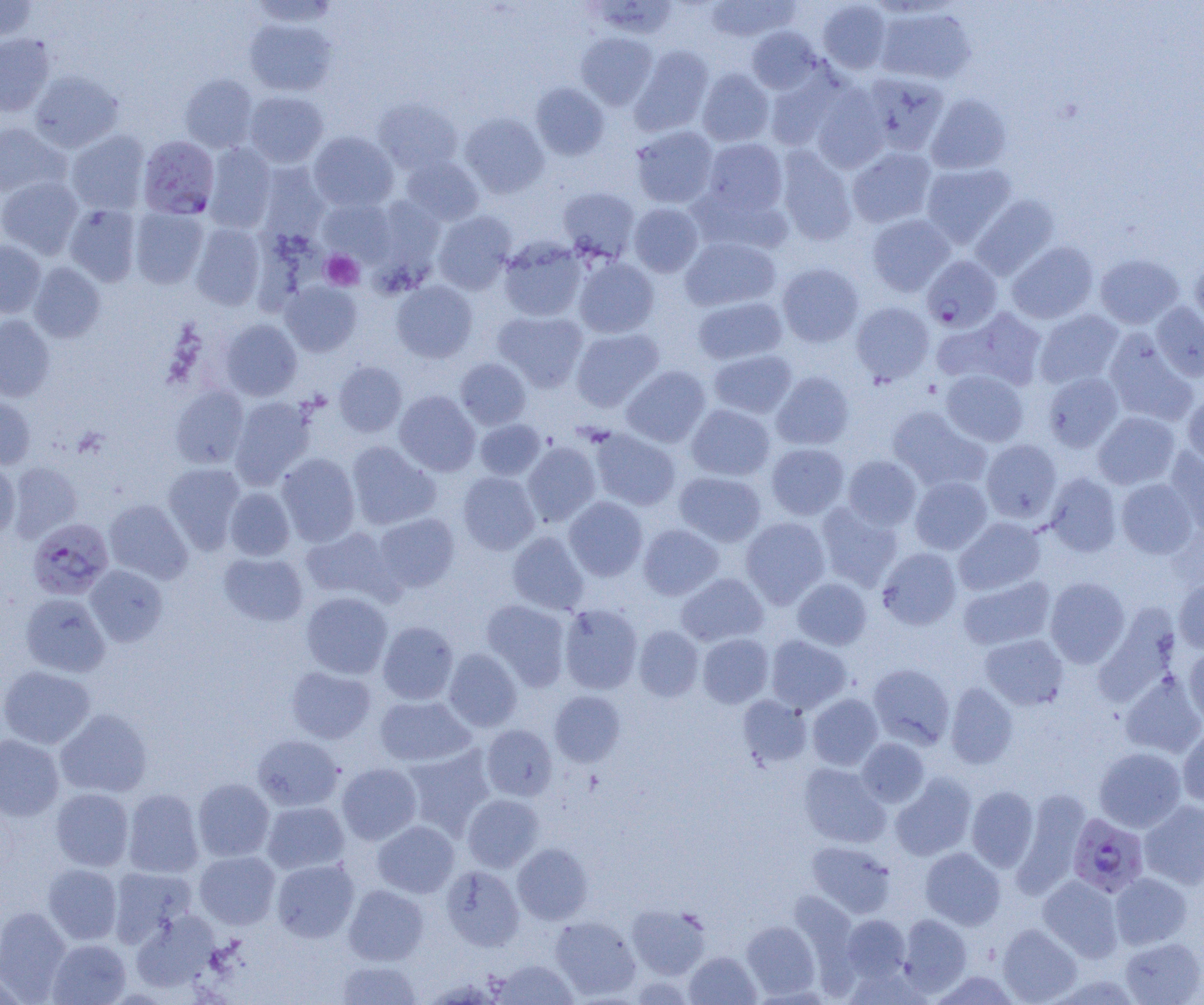
Summary:
  - Coordinate format: approximate bounding boxes as [x1, y1, x2, y2] in pixels
  - Uninfected red blood cell locations (subset): [0, 0, 37, 42], [247, 0, 337, 27], [587, 0, 680, 40], [705, 0, 799, 42], [817, 1, 892, 74], [874, 6, 977, 85], [243, 19, 337, 96], [746, 26, 823, 94], [576, 32, 657, 110], [0, 34, 55, 116], [630, 45, 713, 135], [697, 68, 774, 147], [764, 68, 846, 151], [29, 71, 123, 152], [861, 71, 950, 154], [180, 74, 257, 152], [530, 82, 610, 160], [810, 83, 890, 173], [243, 91, 329, 168], [926, 94, 1012, 174], [373, 98, 462, 174], [459, 112, 549, 198], [0, 122, 68, 197], [631, 126, 719, 209], [66, 130, 150, 214], [308, 131, 398, 211], [702, 138, 788, 216], [203, 143, 277, 232], [775, 146, 857, 245], [847, 146, 937, 228], [400, 156, 484, 226], [921, 162, 1016, 248], [257, 163, 329, 243], [0, 176, 83, 258], [557, 186, 640, 263], [970, 194, 1060, 280], [318, 197, 395, 264], [628, 202, 704, 277], [64, 204, 141, 286], [130, 207, 208, 289], [433, 210, 517, 294], [866, 213, 955, 297], [190, 222, 266, 310], [681, 236, 781, 311], [498, 238, 588, 322], [0, 240, 46, 317], [1006, 241, 1099, 324], [1095, 254, 1184, 329], [573, 257, 659, 338], [1190, 260, 1204, 334], [28, 262, 106, 342], [777, 263, 864, 347], [391, 280, 478, 363], [280, 281, 362, 356], [692, 296, 787, 365], [851, 301, 934, 385], [1151, 302, 1204, 381], [938, 307, 1049, 392], [1034, 309, 1124, 389], [493, 310, 588, 392], [0, 315, 55, 401], [220, 319, 302, 401], [571, 327, 664, 412], [1103, 331, 1198, 425], [709, 349, 798, 418], [455, 358, 531, 430], [333, 361, 407, 437], [621, 365, 711, 448], [941, 370, 1029, 446], [771, 371, 855, 450], [1043, 372, 1123, 454], [170, 385, 249, 468], [394, 390, 480, 476], [1182, 391, 1204, 466], [0, 394, 35, 469], [230, 396, 316, 489], [686, 404, 775, 481], [887, 406, 991, 492], [1093, 411, 1180, 489], [475, 419, 545, 480], [590, 428, 680, 511], [981, 439, 1062, 523], [346, 441, 439, 530], [521, 441, 601, 525], [766, 443, 849, 520], [1164, 448, 1204, 535], [276, 453, 361, 546], [842, 455, 922, 530], [0, 460, 20, 538], [8, 461, 82, 542], [162, 463, 246, 553], [674, 471, 766, 546], [457, 472, 540, 554], [1045, 472, 1122, 556], [910, 476, 992, 554], [1116, 478, 1198, 558], [224, 487, 295, 560], [564, 497, 648, 581], [104, 499, 193, 584], [815, 502, 902, 591], [374, 513, 460, 594], [740, 517, 830, 607], [954, 517, 1045, 595], [638, 524, 723, 600], [301, 526, 397, 602], [507, 531, 589, 615], [877, 547, 961, 629], [218, 552, 307, 626], [84, 565, 167, 646], [676, 573, 768, 646], [958, 575, 1055, 650], [792, 577, 872, 649], [1045, 577, 1130, 667], [1174, 579, 1204, 653], [301, 591, 393, 679], [21, 593, 110, 677], [481, 600, 571, 690], [559, 604, 643, 694], [378, 621, 458, 704], [633, 625, 704, 701], [697, 634, 773, 708], [980, 634, 1068, 710], [765, 635, 851, 713], [1184, 646, 1204, 728], [443, 648, 522, 732], [867, 663, 955, 748], [0, 666, 96, 749], [286, 666, 376, 744], [1120, 672, 1204, 758], [945, 683, 1018, 769], [549, 691, 625, 766], [807, 694, 883, 770], [738, 695, 812, 768], [374, 696, 474, 767], [55, 708, 153, 798], [481, 724, 557, 801], [1178, 725, 1204, 807], [0, 734, 64, 821], [252, 735, 343, 811], [856, 737, 929, 807], [402, 746, 496, 840], [1094, 747, 1186, 832], [337, 763, 422, 844], [800, 763, 890, 848], [891, 773, 976, 861], [192, 778, 274, 862], [966, 786, 1039, 871], [51, 788, 134, 871], [123, 788, 204, 878], [1012, 788, 1091, 897], [462, 794, 544, 872], [1139, 799, 1204, 888], [262, 801, 349, 873], [372, 820, 459, 897], [807, 841, 896, 917], [513, 843, 593, 924], [920, 847, 1005, 930], [194, 850, 280, 929], [272, 859, 359, 942], [43, 863, 122, 944], [441, 865, 524, 951], [109, 866, 197, 946], [1110, 872, 1192, 949], [1038, 874, 1124, 962], [343, 885, 429, 966], [626, 904, 711, 979], [0, 906, 72, 1001], [131, 909, 220, 993], [898, 914, 972, 994], [841, 915, 910, 981], [551, 916, 641, 999], [741, 920, 820, 999], [997, 923, 1082, 1004], [1119, 937, 1204, 1004], [47, 939, 131, 1005], [684, 951, 760, 1005], [493, 959, 578, 1004], [337, 960, 422, 1004]
  - Plasmodium falciparum-infected red blood cell locations (subset): [138, 135, 220, 219], [27, 517, 113, 600], [1067, 813, 1149, 897]
  - Platelet locations: [321, 250, 364, 290]
  - Slide-level diagnosis: Plasmodium falciparum
  - Modality: light microscopy
  - Field of view: one of a larger specimen
  - Preparation: thin blood film
  - Image size: 1204×1005 pixels
  - Magnification: 1000x